State which parasite is depicted.
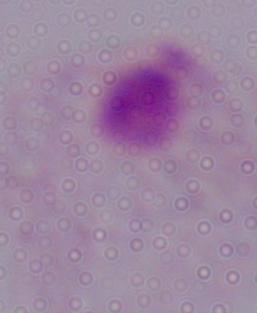
A trichomonad.

Micrograph. 1000x magnification.